Assess the morphology of the red blood cells.
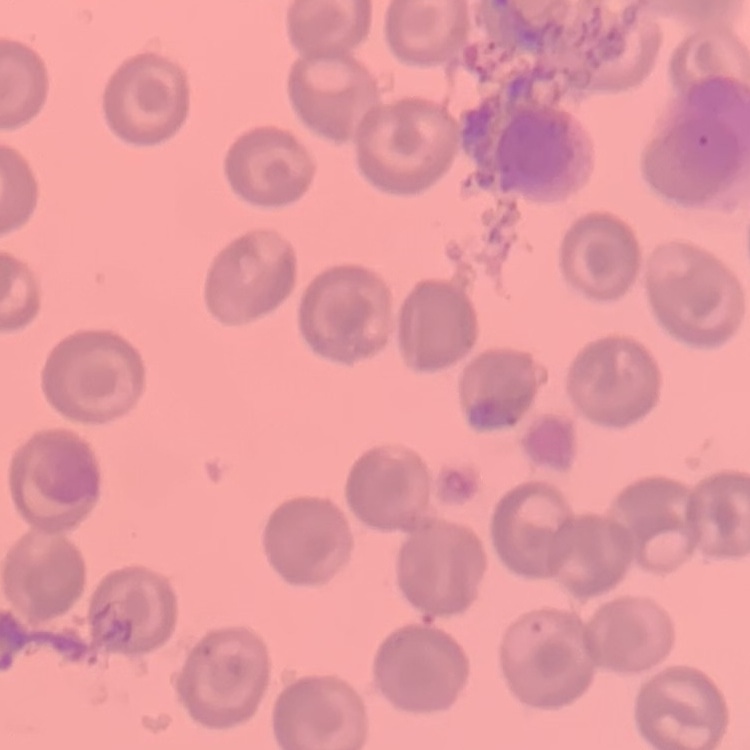

They show no rouleaux formation.

Stained with either Field's or Giemsa. Square crop of a larger photomicrograph. Thin blood film.